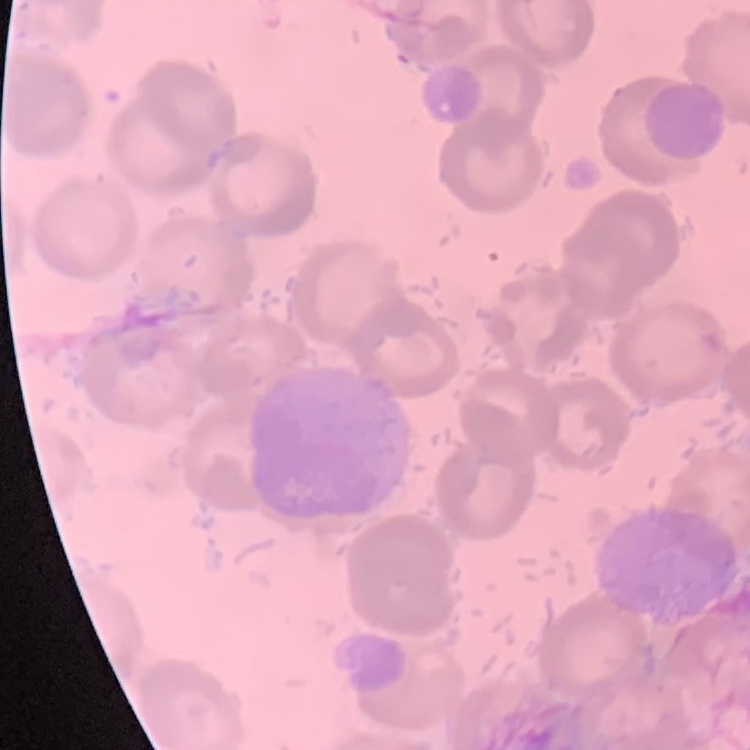
The erythrocytes show no rouleaux formation. Stained with either Field's or Giemsa. Thin blood smear. Square crop of a larger photomicrograph.